State which parasite is depicted.
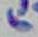
Toxoplasma gondii.

Micrograph. Captured at 1000x magnification.